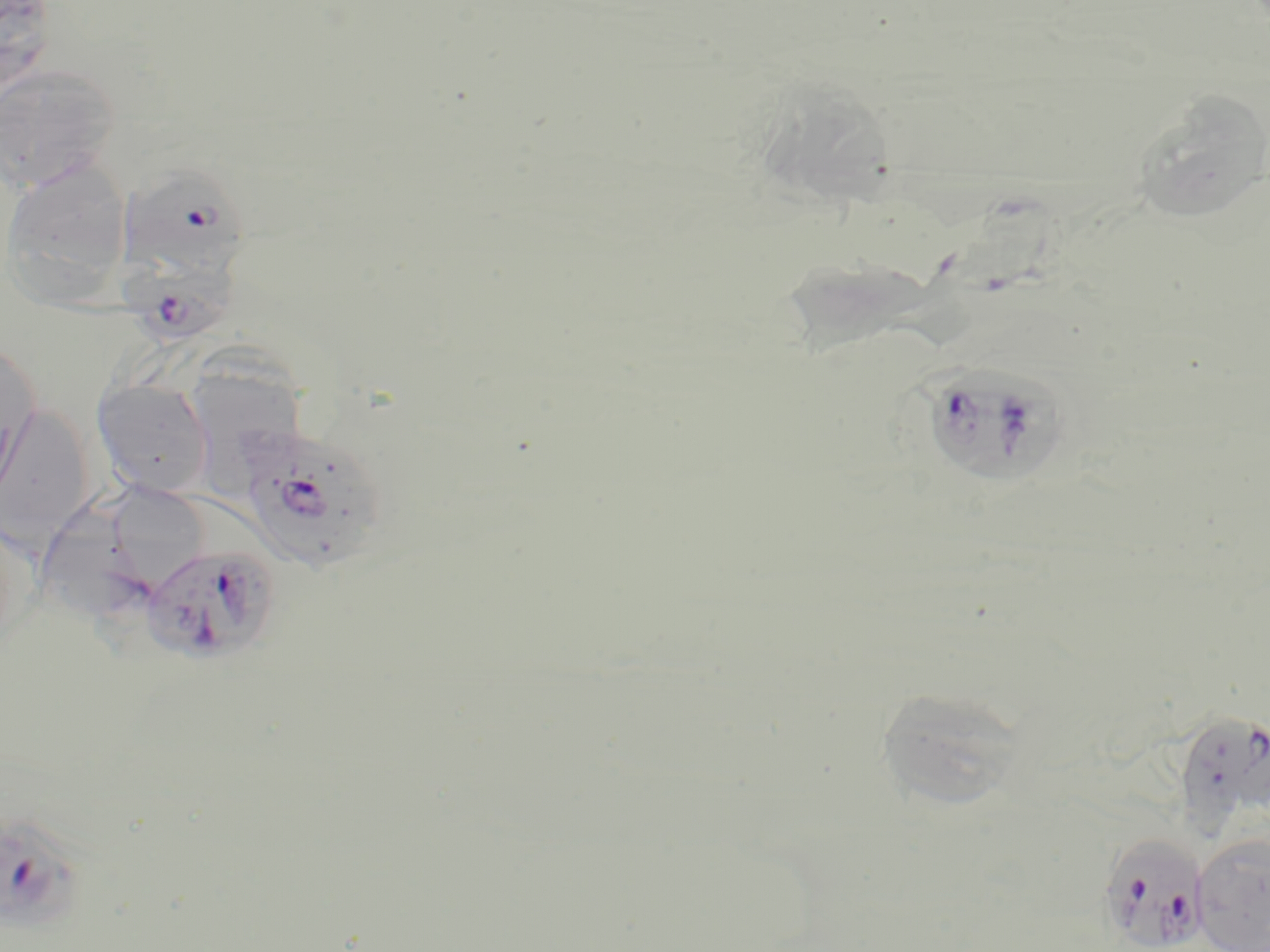
Summary:
  - Coordinate format: approximate bounding boxes as named x1/y1/x2/y2 corners in pixels
  - Plasmodium falciparum-infected red blood cell locations: (x1=129, y1=166, x2=254, y2=276), (x1=122, y1=249, x2=240, y2=347), (x1=922, y1=365, x2=1062, y2=485), (x1=246, y1=428, x2=385, y2=574), (x1=141, y1=544, x2=282, y2=667), (x1=1180, y1=717, x2=1270, y2=835), (x1=0, y1=810, x2=88, y2=937), (x1=1100, y1=823, x2=1210, y2=952)
  - Uninfected red blood cell locations: (x1=1, y1=0, x2=60, y2=98), (x1=0, y1=63, x2=120, y2=194), (x1=757, y1=70, x2=906, y2=209), (x1=1130, y1=90, x2=1270, y2=222), (x1=1, y1=159, x2=135, y2=301), (x1=795, y1=260, x2=983, y2=358), (x1=197, y1=339, x2=314, y2=502), (x1=0, y1=341, x2=40, y2=497), (x1=92, y1=378, x2=215, y2=499), (x1=0, y1=403, x2=96, y2=550), (x1=117, y1=482, x2=204, y2=596), (x1=43, y1=488, x2=145, y2=626), (x1=0, y1=516, x2=33, y2=662), (x1=884, y1=692, x2=1028, y2=812), (x1=1193, y1=833, x2=1270, y2=950)
  - Slide-level diagnosis: Plasmodium falciparum
  - Preparation: thin blood smear
  - Modality: optical microscopy
  - Image size: 1270×952 pixels
  - Field of view: one of a larger specimen
  - Stain: May-Grünwald-Giemsa
  - Magnification: 1000x